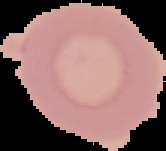
Summary:
  - Image size: 166×151 pixels
  - Image type: segmented cell region with the area outside set to black
  - Preparation: thin blood film
  - Malaria status: uninfected